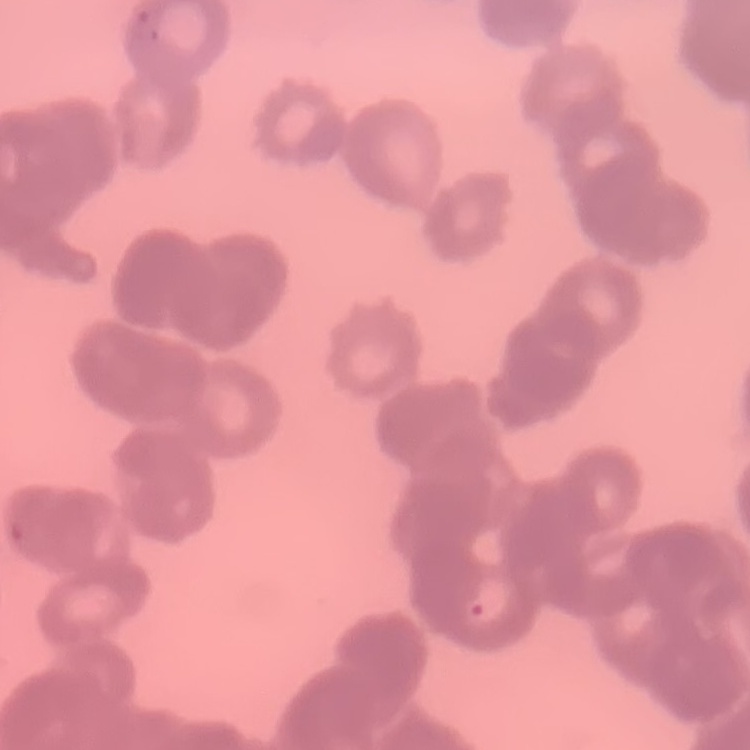

The erythrocytes show rouleaux formation. Field's or Giemsa stain. One tile cut from a larger photomicrograph. Thin blood film.